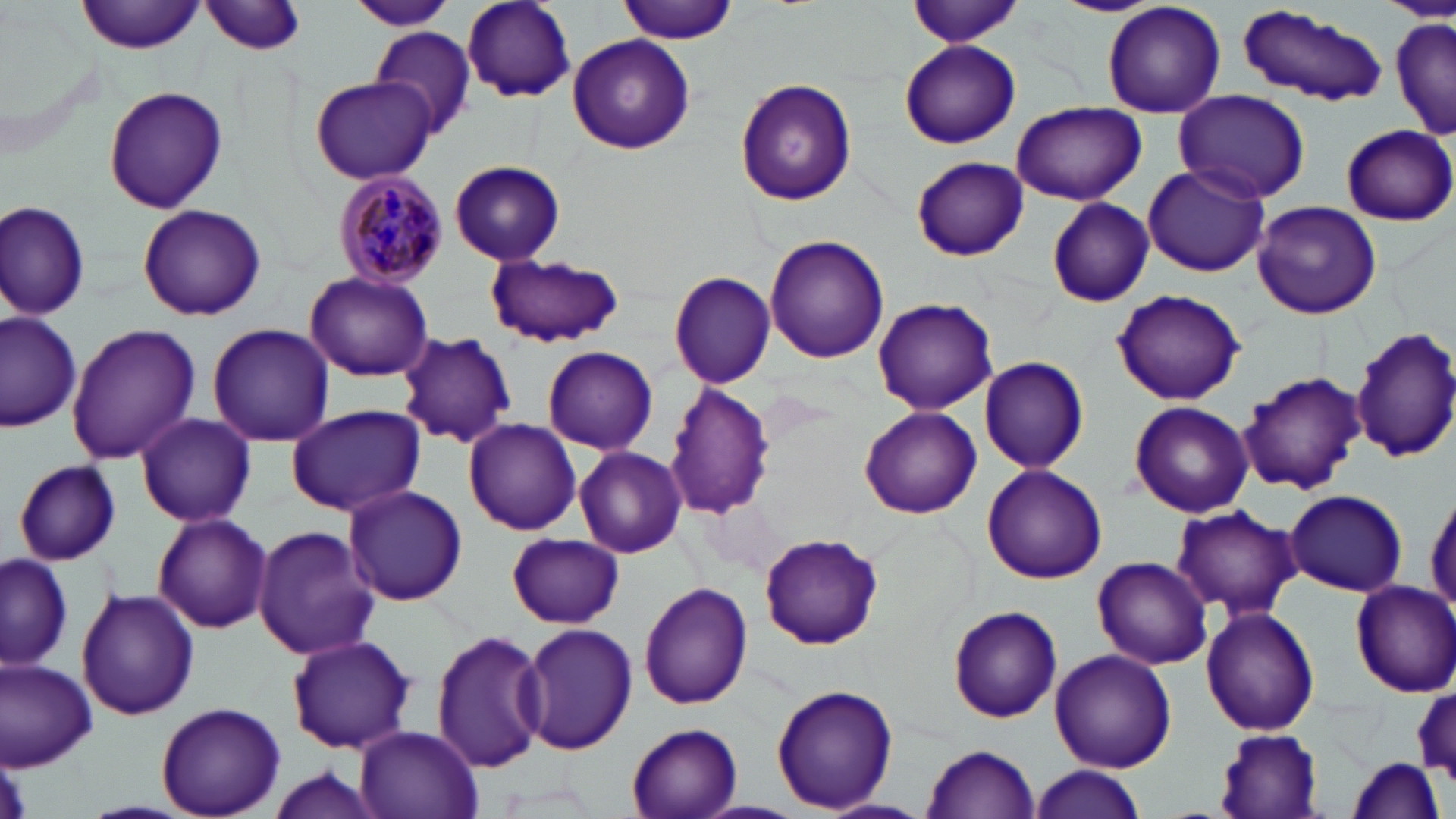

slide-level diagnosis = Plasmodium malariae
field of view = single
magnification = 1000x
Plasmodium malariae-infected red blood cell locations = approximate bounding boxes as (x1, y1, x2, y2) in pixels: (334, 170, 450, 290)
image size = 1456×819 pixels
uninfected red blood cell locations = approximate bounding boxes as (x1, y1, x2, y2) in pixels: (78, 0, 205, 55), (344, 0, 459, 30), (461, 0, 577, 104), (615, 0, 737, 46), (905, 0, 1026, 50), (1051, 0, 1163, 17), (1101, 0, 1227, 117), (201, 1, 308, 57), (1237, 9, 1389, 108), (1390, 15, 1454, 141), (370, 26, 477, 139), (567, 33, 694, 155), (898, 40, 1021, 149), (308, 75, 437, 185), (734, 77, 857, 207), (102, 85, 229, 214), (1171, 88, 1311, 204), (1012, 100, 1145, 205), (1341, 123, 1456, 225), (912, 157, 1028, 262), (450, 160, 566, 266), (1141, 163, 1270, 278), (1, 197, 91, 321), (1045, 197, 1155, 308), (1252, 201, 1383, 320), (137, 205, 266, 322), (765, 235, 889, 362), (483, 253, 627, 348), (305, 271, 434, 382), (667, 271, 775, 389), (1111, 289, 1246, 405), (872, 297, 999, 416), (1, 314, 81, 431), (206, 323, 334, 445), (66, 324, 200, 464), (1349, 325, 1456, 467), (398, 332, 516, 448), (542, 346, 658, 455), (978, 358, 1088, 472), (1240, 370, 1366, 495), (665, 383, 776, 521), (1129, 400, 1253, 518), (284, 405, 426, 516), (860, 406, 982, 518), (135, 414, 256, 526), (463, 418, 582, 535), (573, 447, 687, 558), (13, 459, 122, 565), (982, 463, 1108, 584), (1427, 485, 1456, 621), (342, 486, 468, 606), (1284, 489, 1407, 598), (1170, 504, 1301, 620), (152, 512, 272, 633), (252, 525, 378, 661), (507, 533, 623, 629), (759, 534, 882, 650), (0, 553, 72, 671), (1091, 555, 1213, 670), (1348, 579, 1456, 696), (639, 581, 753, 710), (76, 588, 199, 722), (948, 607, 1062, 723), (1201, 607, 1320, 737), (516, 622, 637, 758), (432, 630, 547, 773), (285, 633, 416, 755), (1049, 648, 1176, 773), (0, 658, 97, 770), (770, 683, 896, 815), (1413, 684, 1456, 781), (156, 702, 285, 818), (627, 723, 742, 818), (355, 725, 483, 819), (1212, 727, 1327, 818), (922, 744, 1041, 818), (1345, 756, 1447, 819), (1030, 765, 1146, 819), (258, 766, 386, 819)
preparation = thin blood film
stain = May-Grünwald-Giemsa
modality = optical microscopy